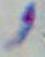

1000x magnification. Toxoplasma gondii is seen. Photomicrograph.